Classify this cell by malaria status.
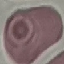
It is uninfected.

Summary:
  - Preparation: thin smear
  - Image type: cell patch, automatically extracted from a larger field of view and resized to 64 × 64 pixels
  - Stain: Giemsa
  - Capture: smartphone through the microscope eyepiece